Classify this cell by malaria status.
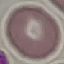

It is uninfected.

preparation = thin blood smear
capture = smartphone camera at the microscope eyepiece
image type = automatically extracted cell patch, resized to 64 × 64 pixels
stain = Giemsa